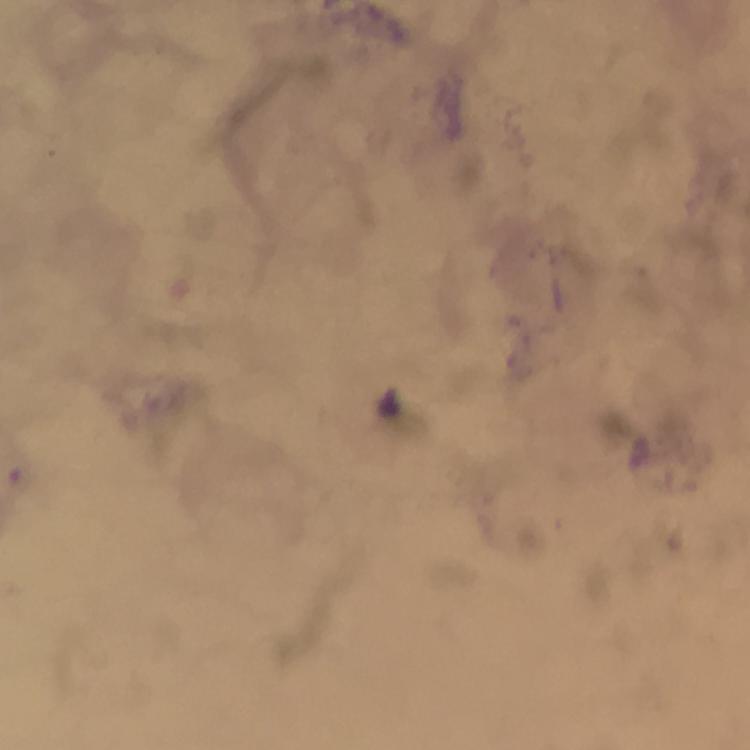 Approximate centers as [x, y] in pixels. Malaria parasite locations: [391, 400]. Immersion oil applied. A crop from one field of view. From a malaria diagnostic workup. Thick smear. Smartphone photograph taken through a microscope. Giemsa-stained preparation. Image is 750×750 pixels. At 100x magnification.